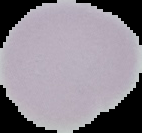

From a thin blood film. Image is 142×133 pixels. The area outside the segmented cell region is set to black. Result: no malaria parasites seen.